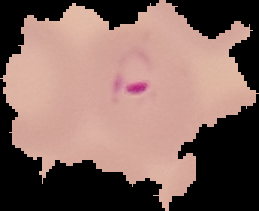
Image is 259×211 pixels. From a thin blood film. Result: malaria parasites identified. Cell region segmented out of the field of view; the surrounding area is masked to black.